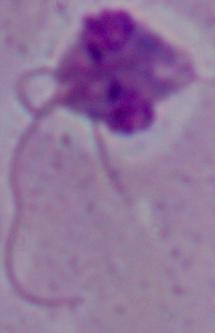
{
  "identification": "Leishmania",
  "magnification": "1000x",
  "modality": "photomicrograph"
}